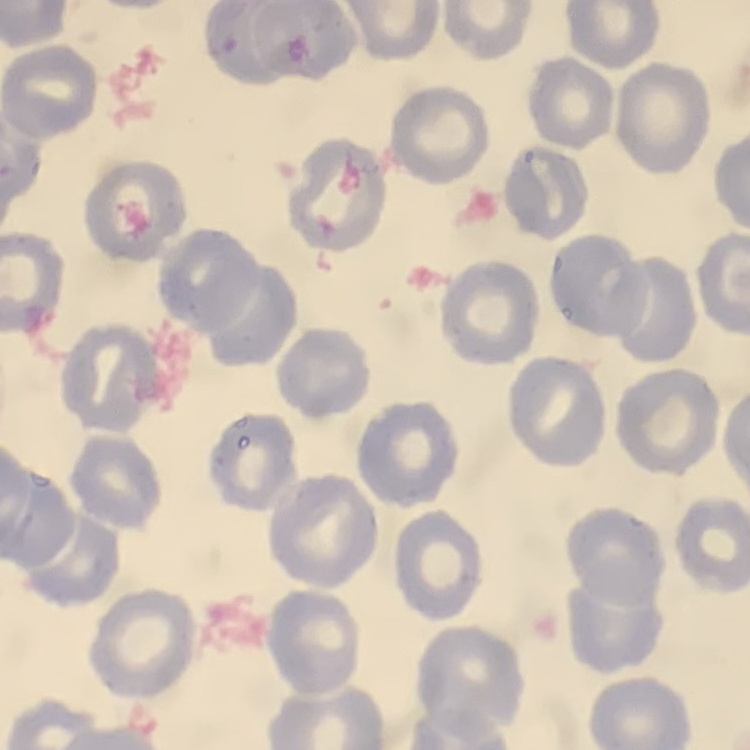

The red blood cells exhibit no rouleaux formation. One tile cut from a larger photomicrograph. Thin blood film. Field's or Giemsa stain.